Assess this cell for malaria.
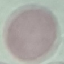
Uninfected.

Summary:
  - Image type: cell patch, automatically extracted from a larger field of view and resized to 64 × 64 pixels
  - Stain: Giemsa
  - Capture: smartphone camera at the microscope eyepiece
  - Preparation: thin blood film